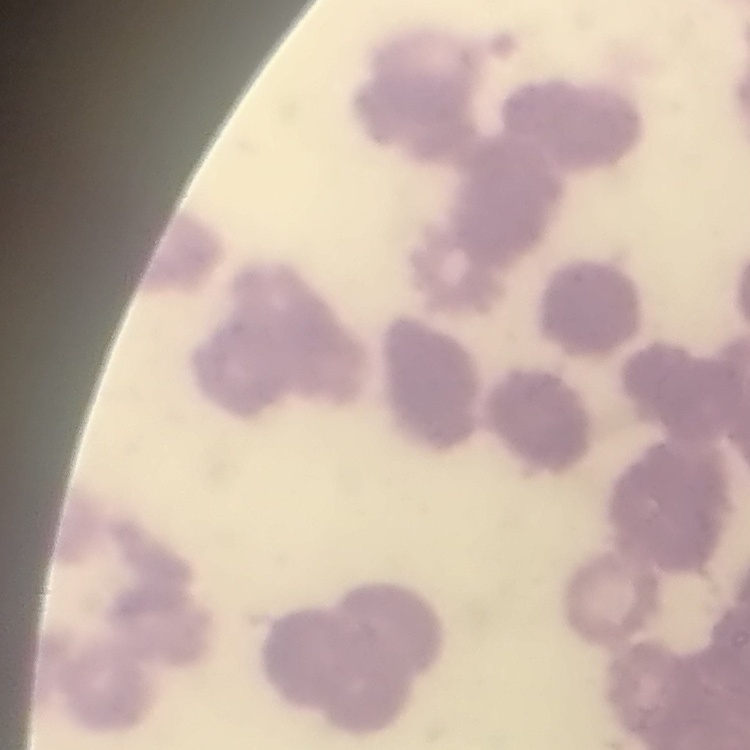

The red blood cells show rouleaux formation. Field's or Giemsa stain. Square crop of a larger photomicrograph. Thin peripheral smear.